State which parasite is depicted.
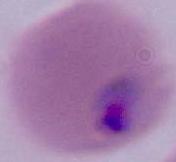
This is Plasmodium.

Photomicrograph. 400x or 1000x magnification.